Assess this cell for malaria.
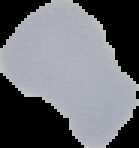
It is uninfected.

Image is 139×148 pixels. Cell region segmented out of the field of view; the surrounding area is masked to black. From a thin blood film.